Comment on the morphology of the red blood cells.
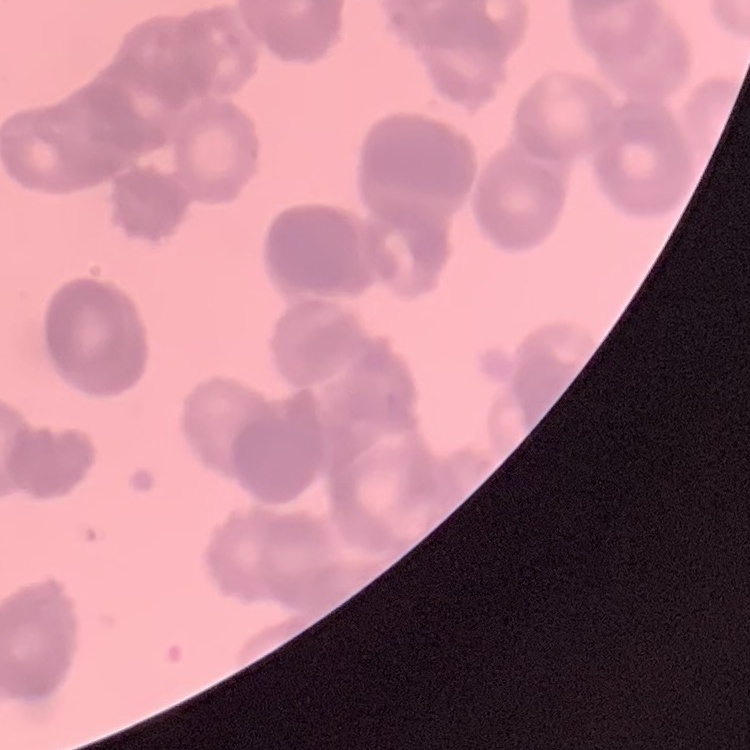

They show rouleaux formation.

Summary:
  - Stain: Field's or Giemsa
  - Preparation: thin blood film
  - Image type: square crop of a larger photomicrograph